Report the malaria status of this cell.
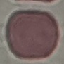

Uninfected.

Cell patch, automatically extracted from a larger field of view and resized to 64 × 64 pixels. Giemsa stain. Acquired by smartphone through the microscope eyepiece. Thin blood smear.